Evaluate for malaria.
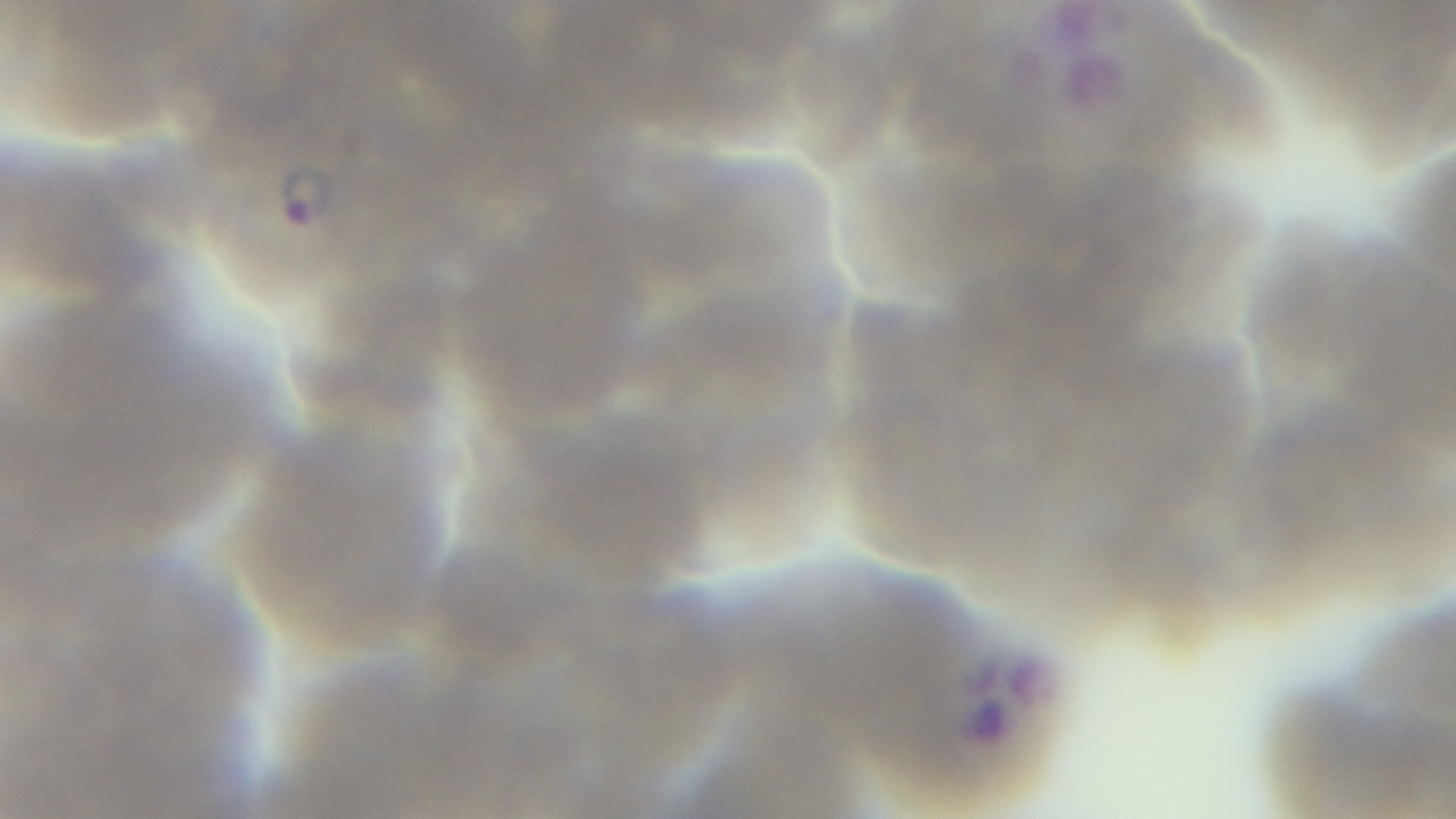
It is infected.

objective = 100x oil immersion
capture = mounted 4K digital camera
stain = Giemsa
preparation = thin
field of view = single
modality = light microscopy